Give the extent of all Plasmodium malariae-infected red blood cells.
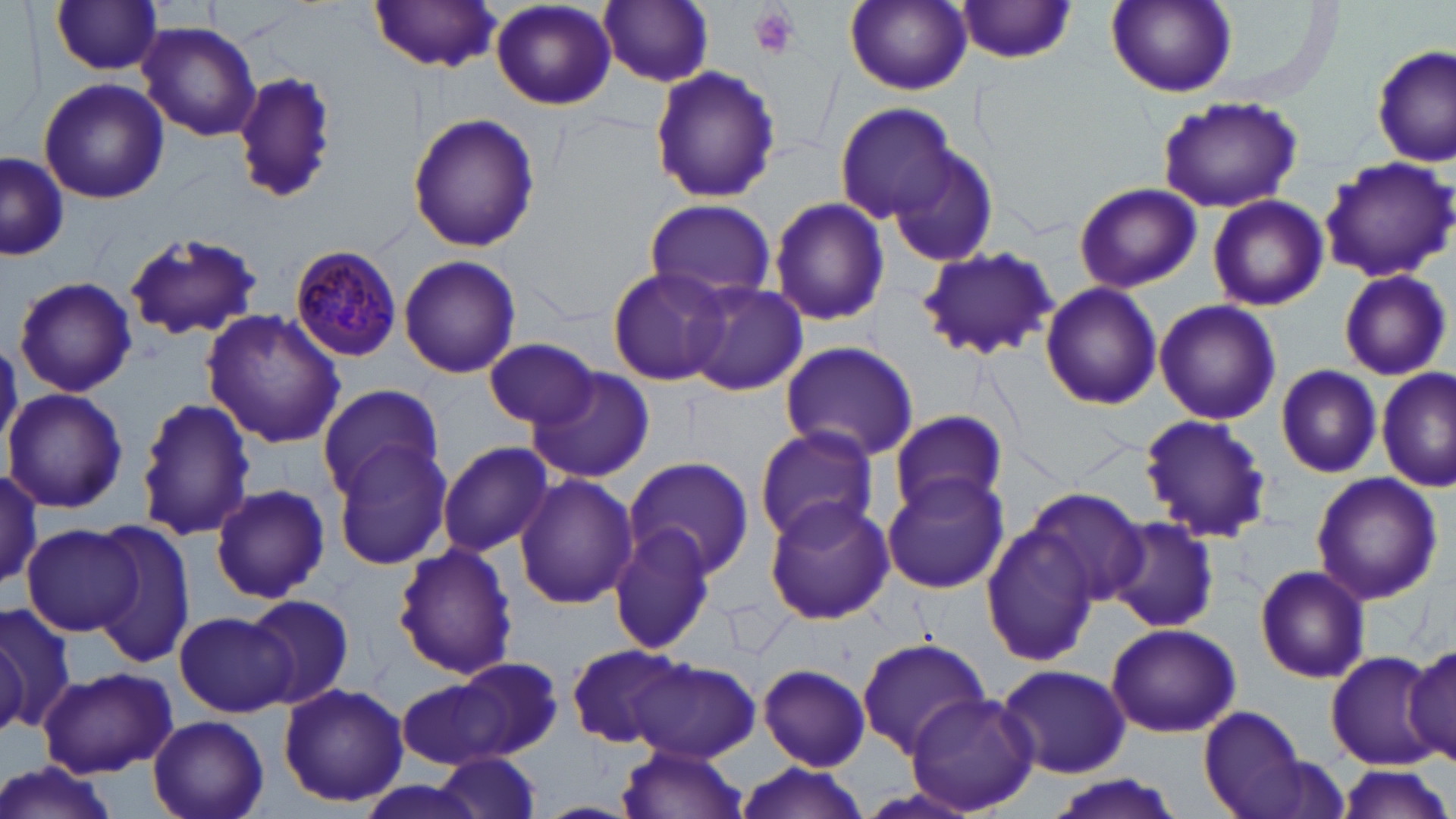
Approximate bounding boxes as (x1,y1)-(x2,y2) corner pairs in pixels.
Plasmodium malariae-infected red blood cells: (288,246)-(403,362).

slide-level diagnosis = Plasmodium malariae
uninfected red blood cell locations = approximate bounding boxes as (x1,y1)-(x2,y2) corner pairs in pixels: (599,0)-(715,87), (844,0)-(974,95), (1106,0)-(1237,98), (48,1)-(166,76), (490,1)-(617,112), (367,2)-(505,72), (955,2)-(1081,65), (138,23)-(261,141), (1372,45)-(1455,167), (648,63)-(781,205), (233,69)-(337,207), (37,77)-(169,204), (1154,95)-(1303,213), (834,102)-(962,227), (408,112)-(539,255), (889,143)-(999,268), (0,153)-(67,260), (1316,155)-(1456,282), (1072,181)-(1202,293), (1206,194)-(1327,311), (767,197)-(889,328), (643,198)-(778,302), (121,230)-(264,343), (915,246)-(1059,363), (398,255)-(522,378), (606,266)-(730,387), (1337,269)-(1451,380), (13,278)-(137,398), (684,280)-(807,396), (1041,283)-(1162,409), (1154,299)-(1282,427), (200,308)-(346,450), (484,338)-(599,429), (778,340)-(921,461), (525,363)-(655,482), (1276,364)-(1384,478), (1377,368)-(1455,493), (316,383)-(443,501), (4,387)-(127,515), (134,396)-(257,543), (889,408)-(1008,518), (1139,414)-(1275,542), (753,425)-(880,547), (329,439)-(453,571), (438,442)-(554,557), (622,457)-(756,580), (0,467)-(43,593), (1310,471)-(1443,607), (881,473)-(1009,595), (514,474)-(636,610), (210,484)-(330,603), (1024,490)-(1150,609), (764,497)-(895,625), (1103,515)-(1219,634), (982,520)-(1106,668), (609,521)-(720,656), (24,523)-(144,637), (88,523)-(196,667), (392,542)-(518,681), (1253,564)-(1372,684), (246,593)-(356,710), (0,598)-(74,737), (173,611)-(296,718), (0,616)-(32,737), (1104,621)-(1242,737), (857,641)-(991,757), (566,642)-(690,750), (1402,645)-(1456,762), (1325,649)-(1448,767), (431,656)-(564,764), (626,657)-(761,763), (757,664)-(871,770), (995,664)-(1132,779), (38,665)-(178,776), (393,677)-(514,772), (277,682)-(408,808), (905,692)-(1041,815), (1197,706)-(1312,817), (148,714)-(268,819), (617,744)-(749,819), (431,754)-(546,817), (1,763)-(122,819), (735,763)-(870,819), (1333,764)-(1452,818), (1041,775)-(1184,819)
platelet locations = approximate bounding boxes as (x1,y1)-(x2,y2) corner pairs in pixels: (747,5)-(799,59)
image size = 1456×819 pixels
modality = light microscopy
magnification = 1000x
preparation = thin blood film
stain = May-Grünwald-Giemsa
field of view = single